Report the malaria status of this cell.
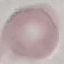

It is uninfected.

Giemsa-stained preparation. Automatically extracted cell patch, resized to 64 × 64 pixels. Thin blood smear. Photographed with a smartphone camera at the microscope eyepiece.